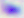
identification = Toxoplasma gondii
modality = photomicrograph
magnification = 400x